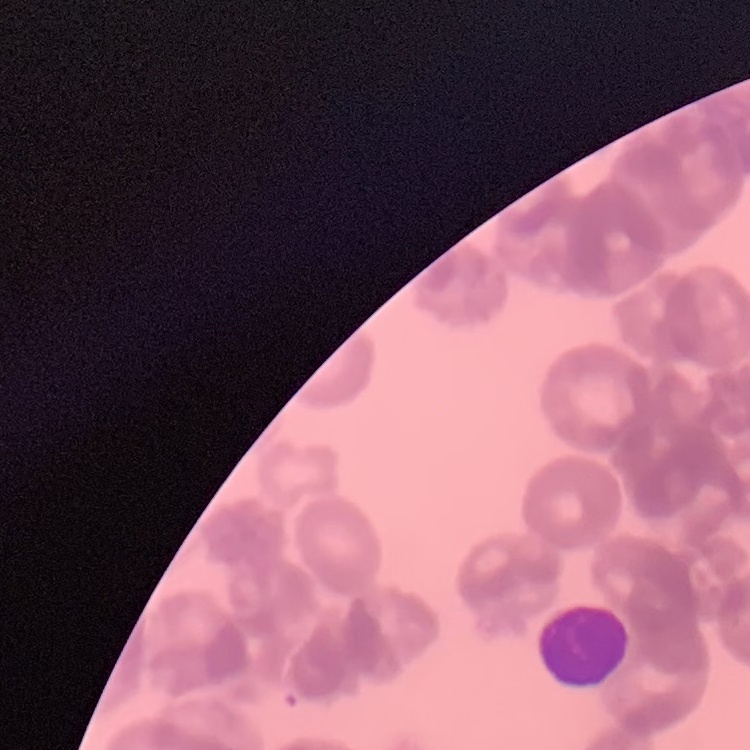
Summary:
  - Red blood cell morphology: rouleaux formation
  - Preparation: thin peripheral smear
  - Stain: Field's or Giemsa
  - Image type: square crop of a larger photomicrograph